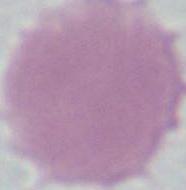
modality = micrograph
identification = red blood cell
magnification = 1000x